Look for Plasmodium parasites.
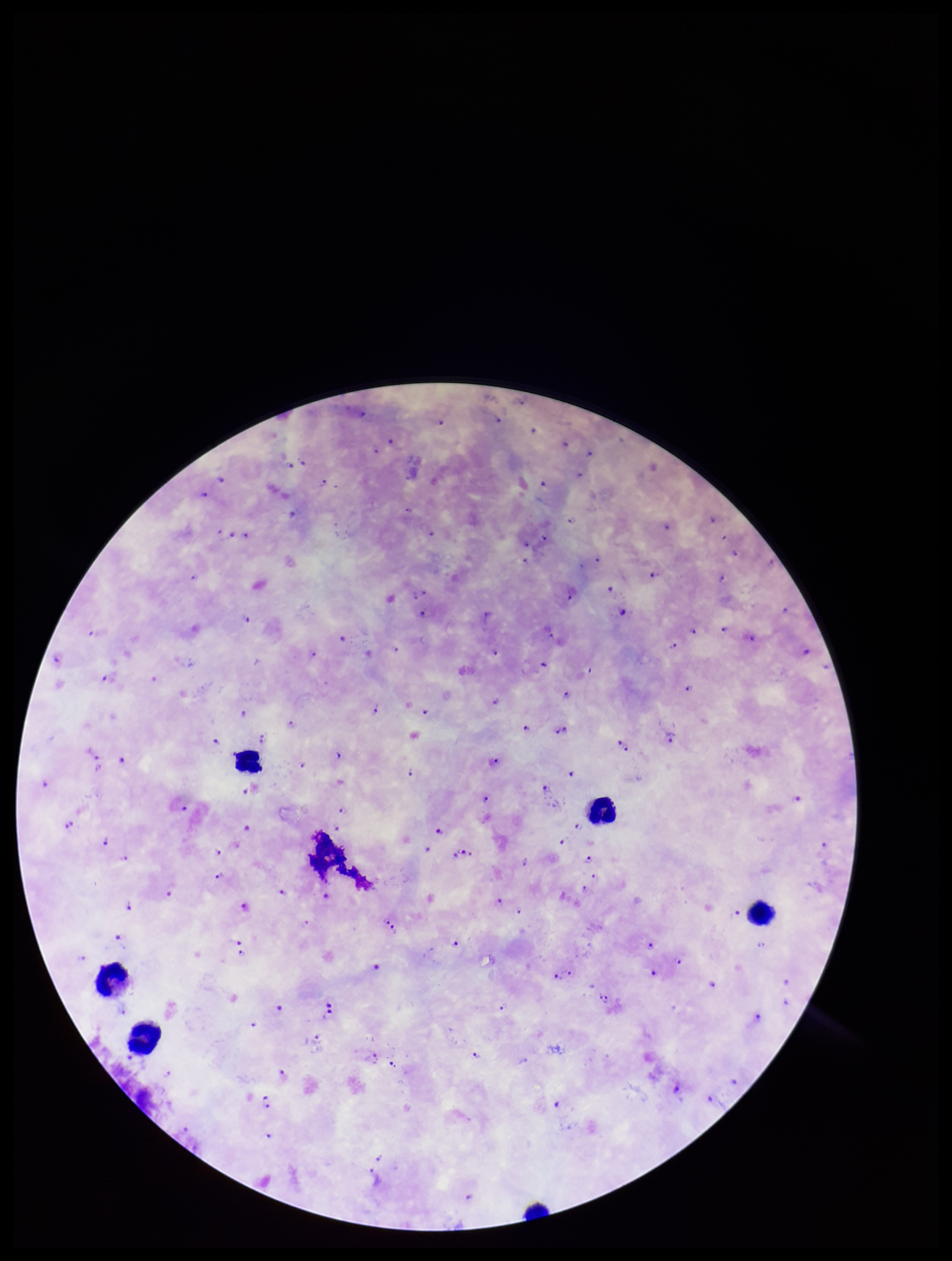
Identified.

Summary:
  - Leukocyte count: 5
  - Field of view: single
  - Parasite count: 100
  - Image size: 952×1261 pixels
  - Patient malaria status: infected
  - Capture: smartphone photograph through the microscope eyepiece
  - Species reported for this patient: Plasmodium falciparum
  - Stain: Giemsa
  - Preparation: thick smear